Outline each Plasmodium falciparum-infected red blood cell.
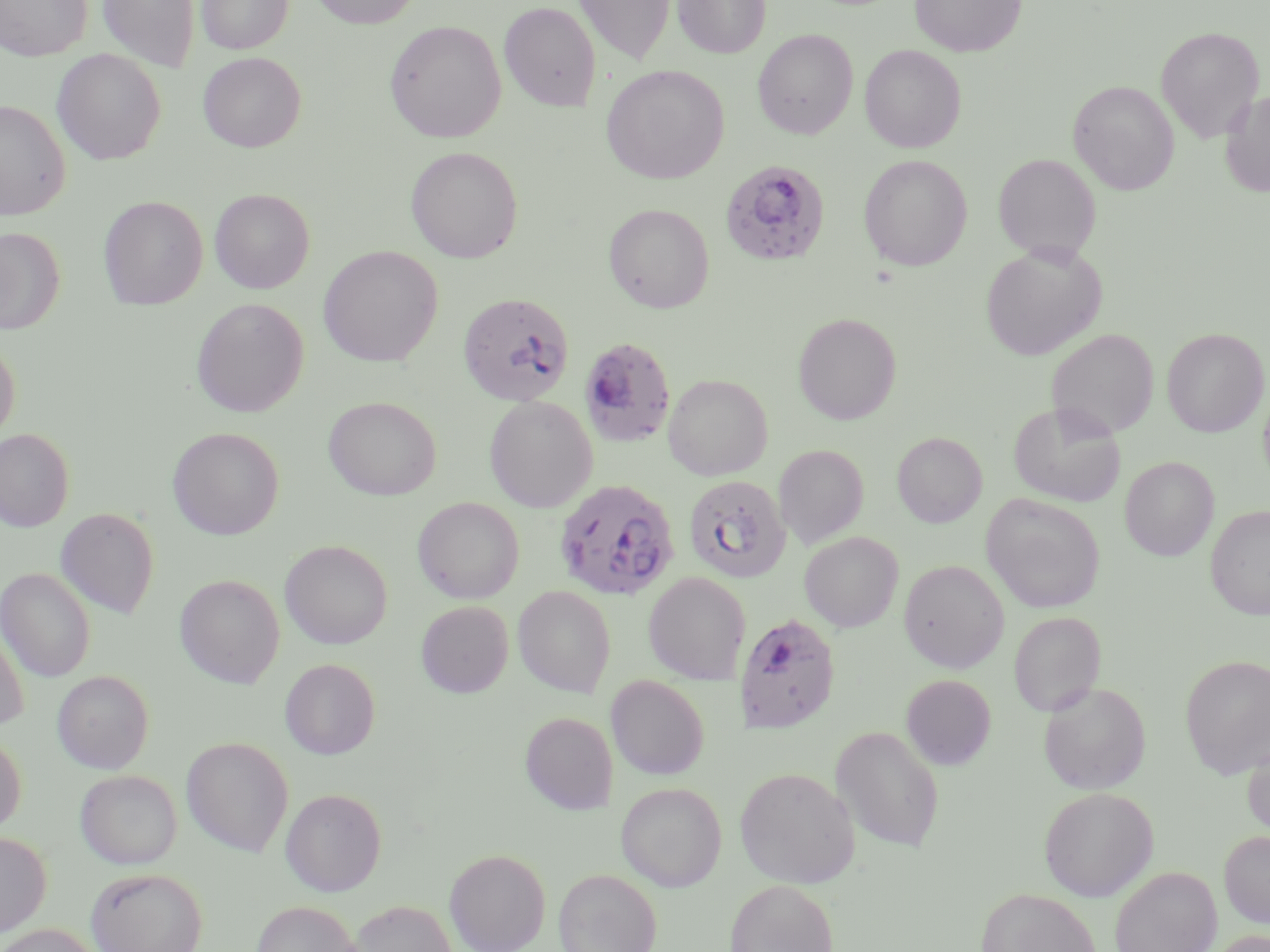
Approximate bounding boxes as named x1/y1/x2/y2 corners in pixels.
Plasmodium falciparum-infected red blood cells: (x1=720, y1=159, x2=830, y2=267), (x1=458, y1=292, x2=575, y2=406), (x1=579, y1=335, x2=677, y2=448), (x1=683, y1=474, x2=791, y2=583), (x1=554, y1=479, x2=679, y2=600), (x1=737, y1=612, x2=840, y2=733).

slide_level_diagnosis: Plasmodium falciparum
magnification: 1000x
modality: light microscopy
preparation: thin blood film
stain: May-Grünwald-Giemsa
field_of_view: single
uninfected_red_blood_cell_locations: 'approximate bounding boxes as named x1/y1/x2/y2 corners in pixels: (x1=0, y1=0, x2=91, y2=61), (x1=97, y1=0, x2=200, y2=72), (x1=197, y1=0, x2=294, y2=54), (x1=309, y1=0, x2=423, y2=29), (x1=572, y1=0, x2=675, y2=65), (x1=673, y1=0, x2=771, y2=58), (x1=909, y1=0, x2=1026, y2=57), (x1=499, y1=1, x2=602, y2=112), (x1=385, y1=20, x2=506, y2=143), (x1=1155, y1=26, x2=1264, y2=142), (x1=753, y1=29, x2=858, y2=139), (x1=860, y1=44, x2=966, y2=153), (x1=51, y1=49, x2=166, y2=165), (x1=198, y1=52, x2=306, y2=152), (x1=601, y1=65, x2=729, y2=184), (x1=1068, y1=80, x2=1179, y2=195), (x1=1220, y1=89, x2=1270, y2=197), (x1=0, y1=99, x2=70, y2=222), (x1=405, y1=146, x2=523, y2=263), (x1=993, y1=153, x2=1100, y2=262), (x1=859, y1=154, x2=972, y2=271), (x1=209, y1=188, x2=315, y2=293), (x1=99, y1=196, x2=208, y2=310), (x1=604, y1=203, x2=715, y2=313), (x1=1, y1=227, x2=65, y2=334), (x1=981, y1=243, x2=1107, y2=361), (x1=318, y1=246, x2=443, y2=367), (x1=191, y1=297, x2=309, y2=417), (x1=793, y1=312, x2=902, y2=424), (x1=1162, y1=328, x2=1269, y2=437), (x1=1047, y1=329, x2=1158, y2=439), (x1=0, y1=340, x2=20, y2=442), (x1=663, y1=373, x2=772, y2=480), (x1=1258, y1=385, x2=1270, y2=489), (x1=484, y1=395, x2=597, y2=512), (x1=323, y1=396, x2=441, y2=500), (x1=1008, y1=401, x2=1126, y2=507), (x1=167, y1=427, x2=284, y2=540), (x1=0, y1=428, x2=74, y2=532), (x1=892, y1=432, x2=987, y2=527), (x1=774, y1=444, x2=869, y2=548), (x1=1120, y1=457, x2=1219, y2=561), (x1=982, y1=493, x2=1105, y2=613), (x1=412, y1=497, x2=524, y2=603), (x1=1206, y1=505, x2=1270, y2=620), (x1=56, y1=507, x2=159, y2=619), (x1=799, y1=532, x2=903, y2=632), (x1=279, y1=539, x2=392, y2=649), (x1=899, y1=559, x2=1009, y2=673), (x1=0, y1=567, x2=95, y2=681), (x1=643, y1=571, x2=751, y2=683), (x1=175, y1=574, x2=285, y2=689), (x1=513, y1=585, x2=616, y2=698), (x1=416, y1=600, x2=513, y2=698), (x1=1008, y1=612, x2=1106, y2=717), (x1=0, y1=620, x2=30, y2=730), (x1=1180, y1=654, x2=1270, y2=778), (x1=279, y1=658, x2=380, y2=759), (x1=52, y1=670, x2=154, y2=774), (x1=900, y1=674, x2=996, y2=770), (x1=605, y1=675, x2=710, y2=780), (x1=1038, y1=681, x2=1151, y2=794), (x1=520, y1=711, x2=617, y2=814), (x1=830, y1=725, x2=946, y2=853), (x1=0, y1=733, x2=26, y2=834), (x1=181, y1=736, x2=293, y2=857), (x1=1242, y1=736, x2=1270, y2=839), (x1=734, y1=767, x2=860, y2=889), (x1=75, y1=769, x2=182, y2=869), (x1=616, y1=781, x2=727, y2=891), (x1=1039, y1=786, x2=1158, y2=902), (x1=281, y1=788, x2=386, y2=896), (x1=1219, y1=830, x2=1270, y2=928), (x1=0, y1=831, x2=52, y2=937), (x1=444, y1=848, x2=551, y2=952), (x1=1110, y1=865, x2=1222, y2=952), (x1=85, y1=866, x2=208, y2=952), (x1=553, y1=868, x2=662, y2=952), (x1=725, y1=878, x2=838, y2=952), (x1=974, y1=887, x2=1103, y2=952), (x1=347, y1=899, x2=458, y2=951), (x1=251, y1=901, x2=362, y2=952), (x1=0, y1=923, x2=102, y2=952), (x1=1206, y1=929, x2=1270, y2=952)'
image_size: 1270×952 pixels